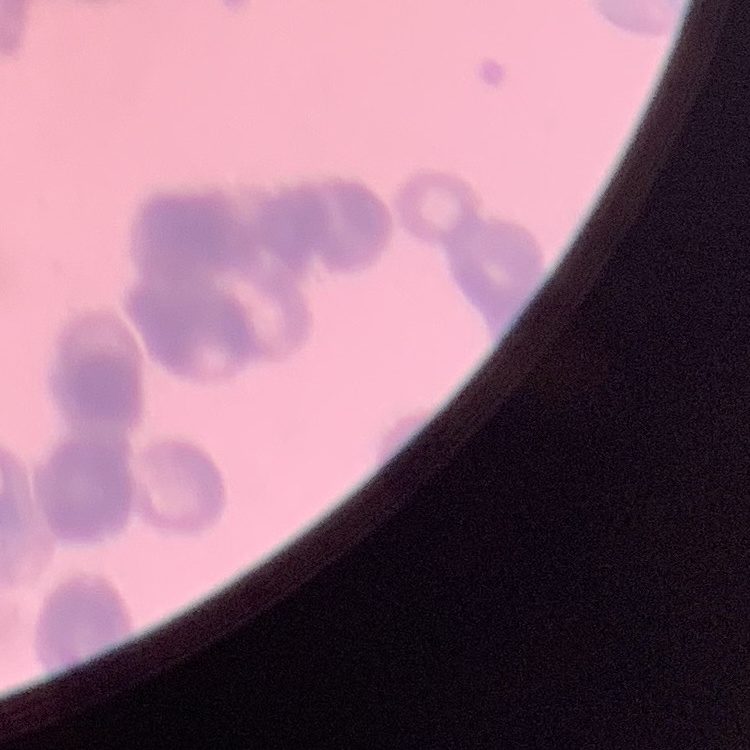

erythrocyte morphology = rouleaux formation
stain = Field's or Giemsa
preparation = thin blood smear
image type = square crop of a larger photomicrograph